Classify this cell by malaria status.
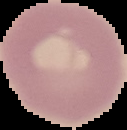
It is uninfected.

Summary:
  - Preparation: thin blood film
  - Image size: 127×130 pixels
  - Image type: segmented cell region on a black background